Comment on the morphology of the red blood cells.
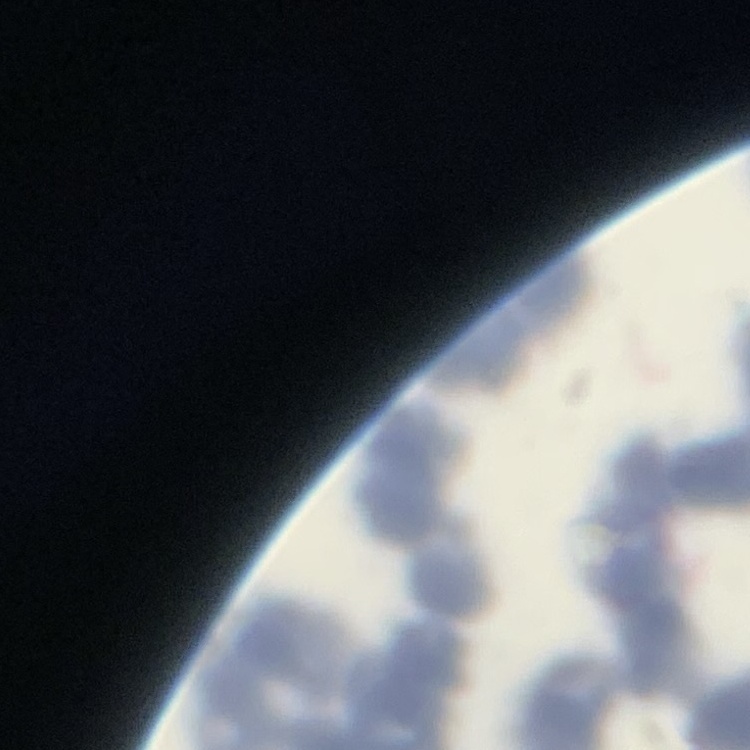

Rouleaux formation.

image_type: square crop of a larger photomicrograph
stain: Field's or Giemsa
preparation: thin blood smear